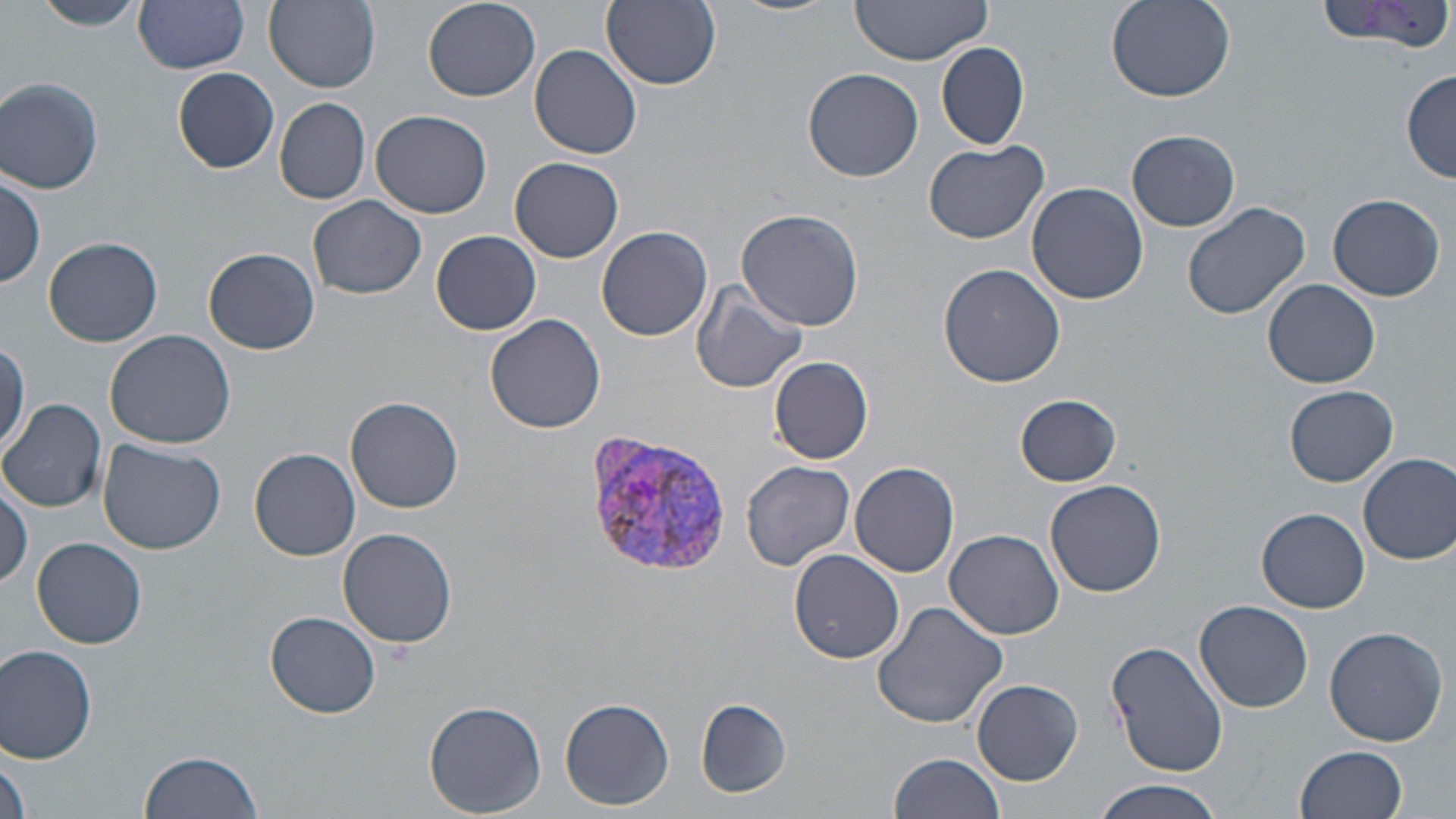
slide-level diagnosis = Plasmodium vivax
modality = optical microscopy
stain = May-Grünwald-Giemsa
field of view = single
uninfected red blood cell locations = approximate bounding boxes as (x1, y1, x2, y2) in pixels: (33, 0, 148, 32), (133, 0, 252, 73), (263, 0, 381, 91), (421, 0, 540, 102), (846, 0, 995, 70), (1104, 0, 1235, 103), (1318, 0, 1456, 58), (601, 1, 722, 90), (935, 41, 1029, 150), (530, 45, 643, 161), (173, 66, 280, 172), (804, 67, 924, 182), (1401, 72, 1456, 181), (1, 77, 103, 194), (274, 98, 370, 204), (371, 109, 492, 218), (1127, 130, 1240, 231), (923, 140, 1052, 244), (511, 157, 624, 263), (0, 171, 45, 290), (1027, 182, 1148, 304), (1327, 193, 1445, 302), (308, 195, 426, 300), (1180, 199, 1313, 321), (737, 206, 865, 331), (597, 225, 713, 341), (432, 230, 542, 335), (44, 237, 163, 347), (204, 248, 320, 354), (940, 264, 1067, 389), (1262, 277, 1380, 388), (690, 282, 808, 394), (484, 314, 606, 433), (105, 327, 239, 448), (0, 342, 27, 456), (770, 357, 874, 463), (1285, 385, 1397, 486), (1015, 395, 1122, 485), (346, 397, 464, 513), (1, 398, 110, 512), (98, 438, 225, 554), (249, 447, 360, 560), (1358, 453, 1456, 564), (740, 460, 855, 570), (850, 462, 958, 577), (1044, 479, 1167, 597), (0, 480, 33, 591), (1256, 507, 1371, 613), (337, 527, 458, 649), (946, 530, 1065, 641), (33, 537, 148, 648), (790, 548, 905, 664), (871, 600, 1007, 728), (1194, 600, 1313, 713), (265, 612, 382, 718), (1324, 626, 1448, 748), (1106, 639, 1229, 777), (1, 644, 99, 765), (972, 678, 1083, 785), (560, 696, 675, 810), (424, 699, 548, 816), (696, 699, 789, 797), (1295, 745, 1409, 819), (138, 750, 262, 819), (888, 753, 1007, 819), (0, 759, 33, 819), (1094, 783, 1224, 819)
Plasmodium vivax-infected red blood cell locations = approximate bounding boxes as (x1, y1, x2, y2) in pixels: (582, 431, 734, 580)
magnification = 1000x
preparation = thin blood smear
image size = 1456×819 pixels